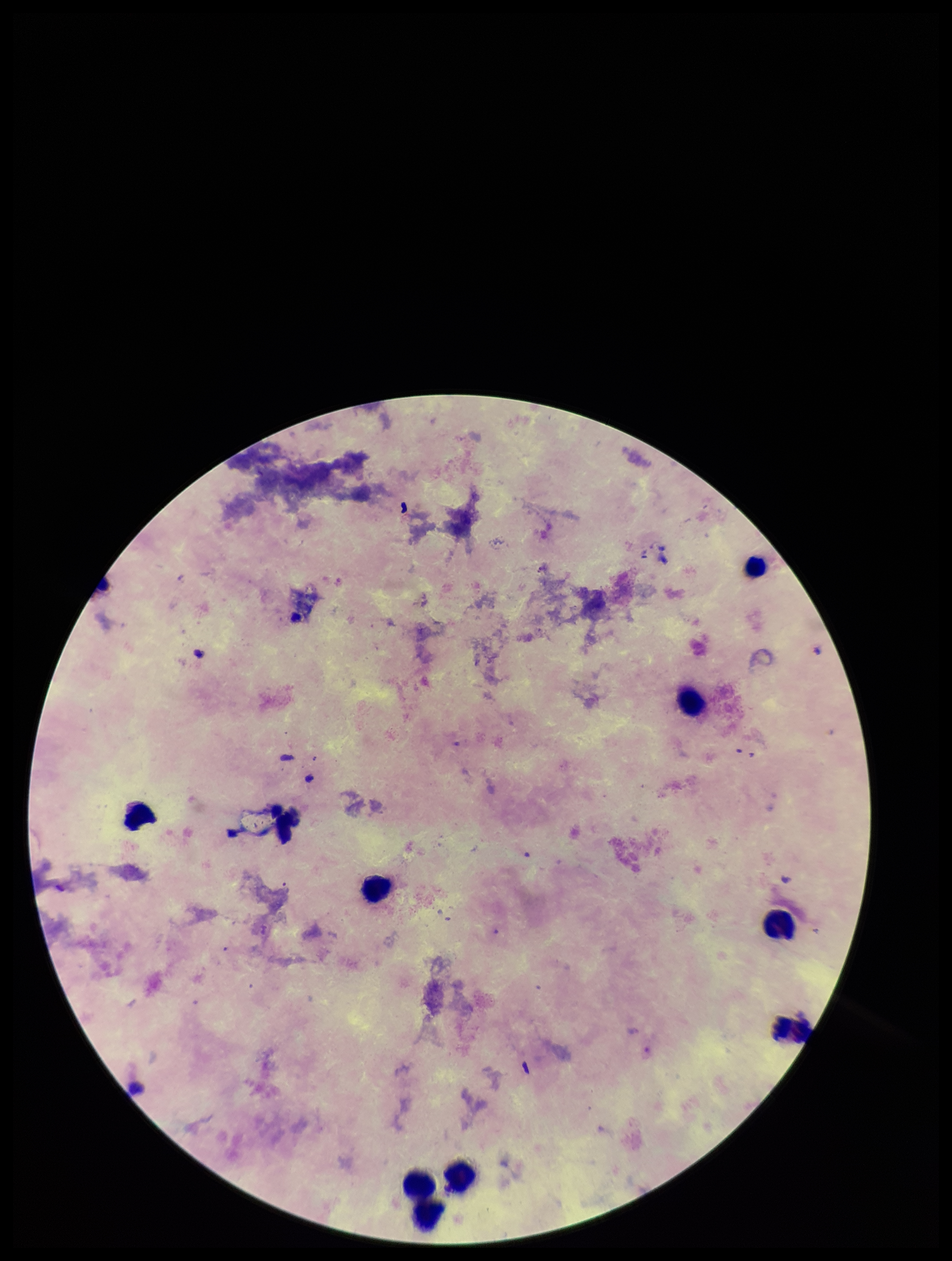

Patient malaria status: negative. Image is 952×1261 pixels. Giemsa stain. Preparation: thick. Plasmodium parasites: none detected. Smartphone photograph taken through the eyepiece of a microscope. Leukocyte count: 9. Single field of view. Parasite count: 0.